Report the malaria status of this cell.
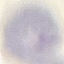
Uninfected.

Giemsa stain. Automatically extracted cell patch, resized to 64 × 64 pixels. Thin smear of blood. Photographed with a smartphone camera at the microscope eyepiece.